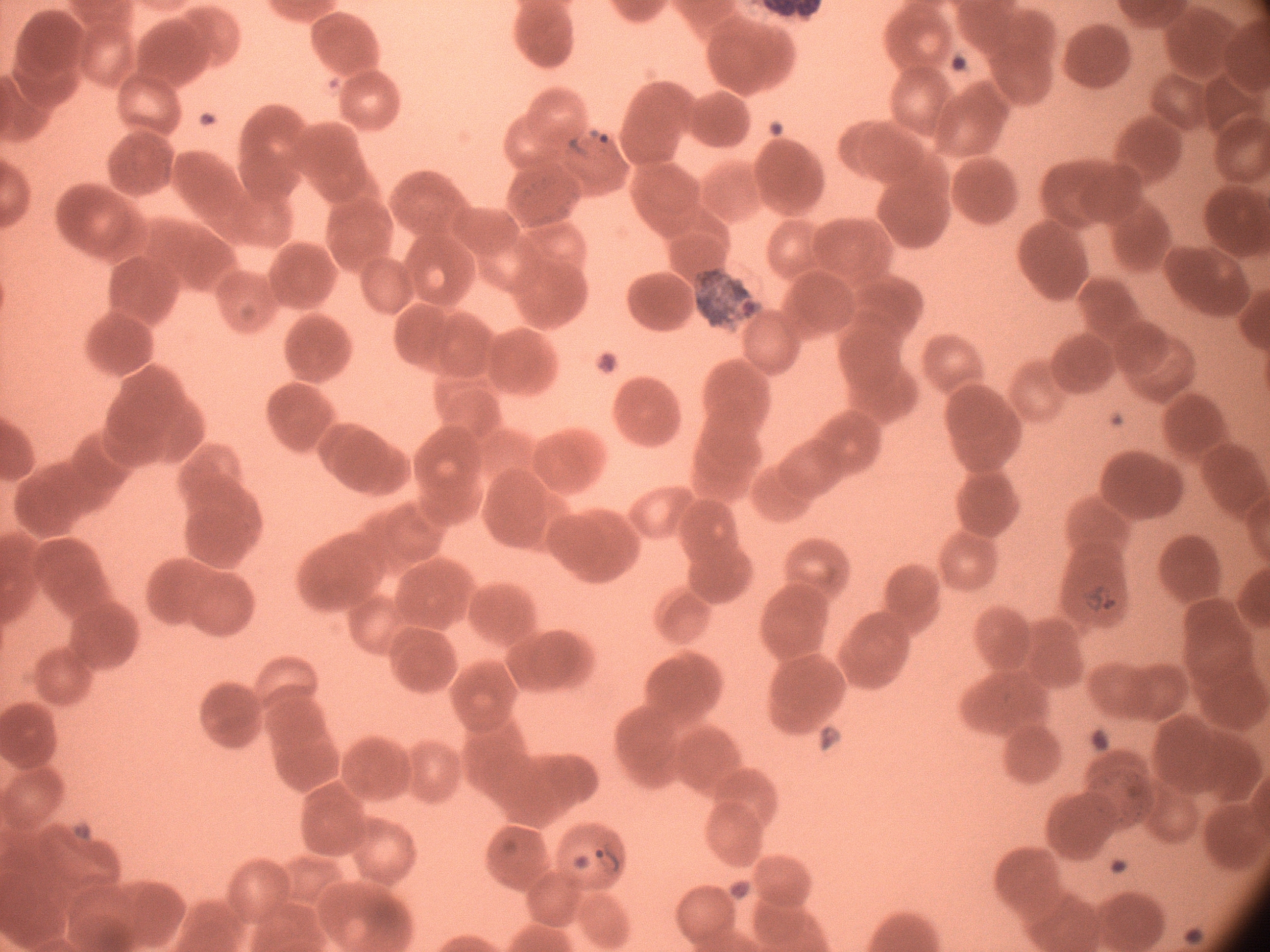
Approximate bounding boxes as (x1, y1, x2, y2) in pixels, from the source annotation, which is not necessarily exhaustive.
Summary:
  - Ring form locations: (567, 126, 612, 161), (1077, 581, 1121, 616), (591, 839, 624, 880)
  - Microscope: Leica DM2000 with built-in camera
  - Preparation: thin blood film
  - Magnification: 100x
  - Species: Plasmodium falciparum
  - Stain: Giemsa
  - Field of view: single
  - Image size: 1270×952 pixels